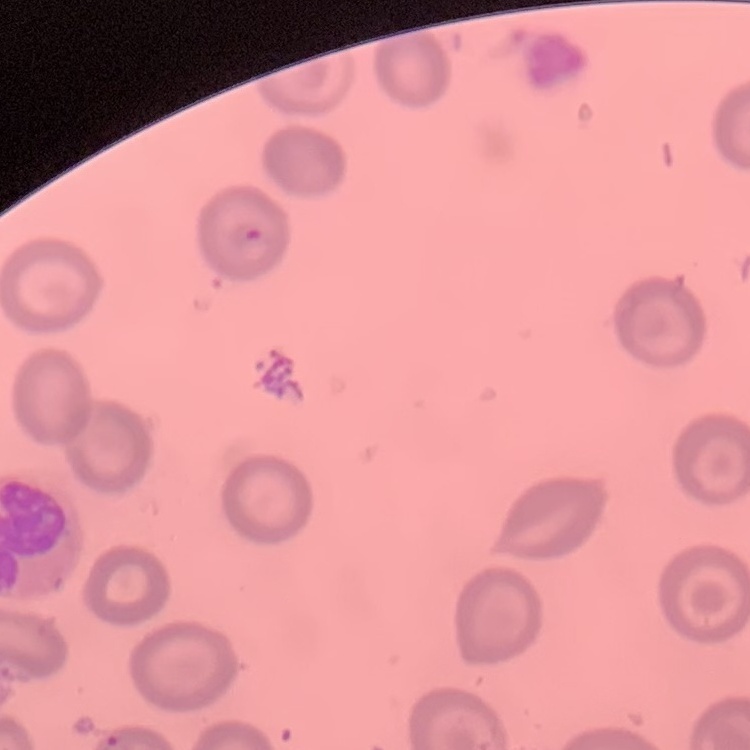

red blood cell morphology = no rouleaux formation
preparation = thin peripheral smear
stain = Field's or Giemsa
image type = square crop of a larger photomicrograph